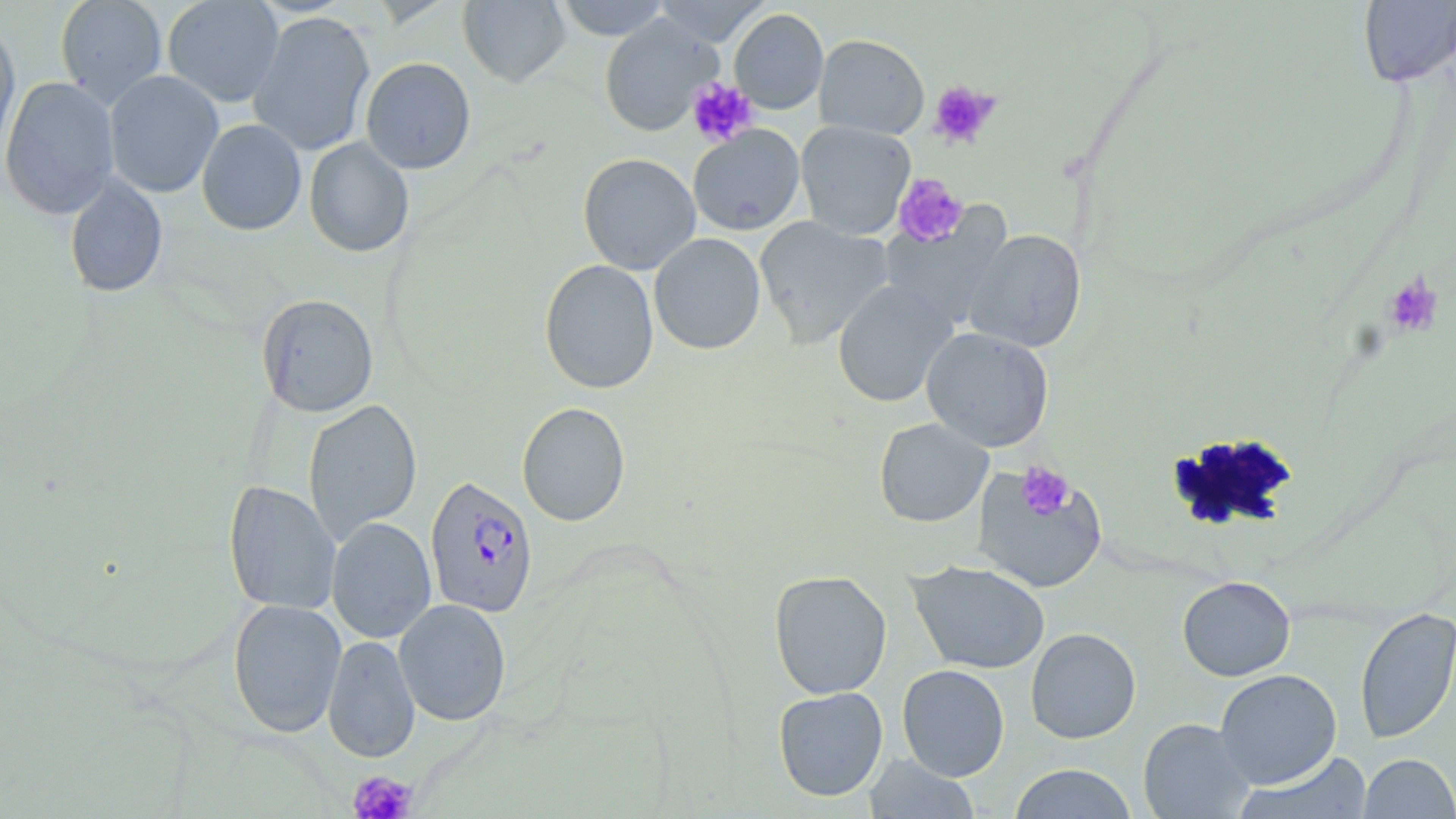

Approximate bounding boxes as [x1, y1, x2, y2] in pixels. Uninfected red blood cell locations: [55, 0, 168, 107], [162, 0, 284, 107], [458, 0, 571, 88], [555, 0, 670, 41], [652, 0, 769, 47], [1358, 0, 1456, 86], [729, 8, 829, 113], [247, 11, 376, 157], [599, 15, 721, 136], [0, 18, 20, 162], [813, 34, 929, 139], [360, 57, 476, 174], [103, 69, 224, 198], [1, 76, 121, 219], [196, 119, 307, 236], [795, 121, 915, 240], [688, 125, 805, 236], [304, 137, 414, 257], [578, 153, 701, 275], [63, 174, 168, 298], [878, 207, 1012, 329], [754, 216, 894, 348], [964, 229, 1086, 352], [649, 233, 766, 354], [539, 259, 659, 394], [832, 279, 958, 407], [256, 293, 379, 417], [921, 327, 1054, 452], [303, 398, 422, 543], [517, 401, 631, 526], [874, 418, 993, 527], [971, 465, 1108, 593], [223, 479, 341, 615], [326, 516, 437, 644], [908, 560, 1050, 674], [768, 569, 892, 700], [1177, 576, 1295, 681], [227, 598, 347, 738], [393, 598, 511, 726], [1354, 606, 1456, 744], [1026, 627, 1141, 744], [322, 634, 420, 763], [896, 664, 1010, 780], [1215, 668, 1342, 788], [773, 687, 888, 801], [1138, 717, 1255, 818], [1232, 751, 1373, 819], [1359, 753, 1456, 818], [863, 754, 982, 818], [1009, 764, 1138, 818]. Platelet locations: [686, 78, 758, 147], [928, 81, 1000, 149], [892, 173, 968, 247], [1384, 274, 1443, 338], [1017, 463, 1075, 519], [348, 769, 418, 819]. Plasmodium falciparum-infected red blood cell locations: [425, 475, 538, 618]. Slide-level diagnosis: Plasmodium falciparum. Single field of view. Image is 1456×819 pixels. Light microscopy. May-Grünwald-Giemsa-stained preparation. 1000x magnification. Thin blood smear.